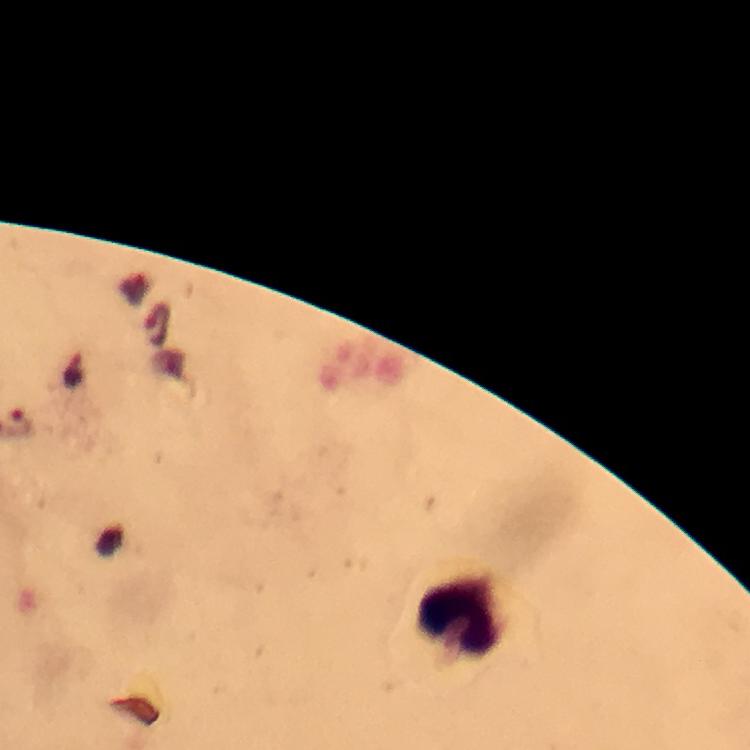 Approximate centers as {x, y} in pixels. Malaria parasite locations: {155, 323}, {73, 370}. Leukocyte locations: {458, 613}. Image is 750×750 pixels. Photographed through the microscope with a smartphone camera. From a diagnostic examination for malaria. Giemsa stain. Thick blood smear. Immersion oil was used. A crop from one field of view. At 100x magnification.